Identify the cell.
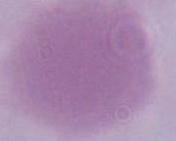

This is an erythrocyte.

modality = micrograph
magnification = 1000x